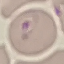

Result: malaria parasites identified. Cell patch, automatically extracted from a larger field of view and resized to 64 × 64 pixels. Giemsa stain. Acquired by smartphone through the microscope eyepiece. Thin blood film.